Give the extent of all Trypanosoma brucei.
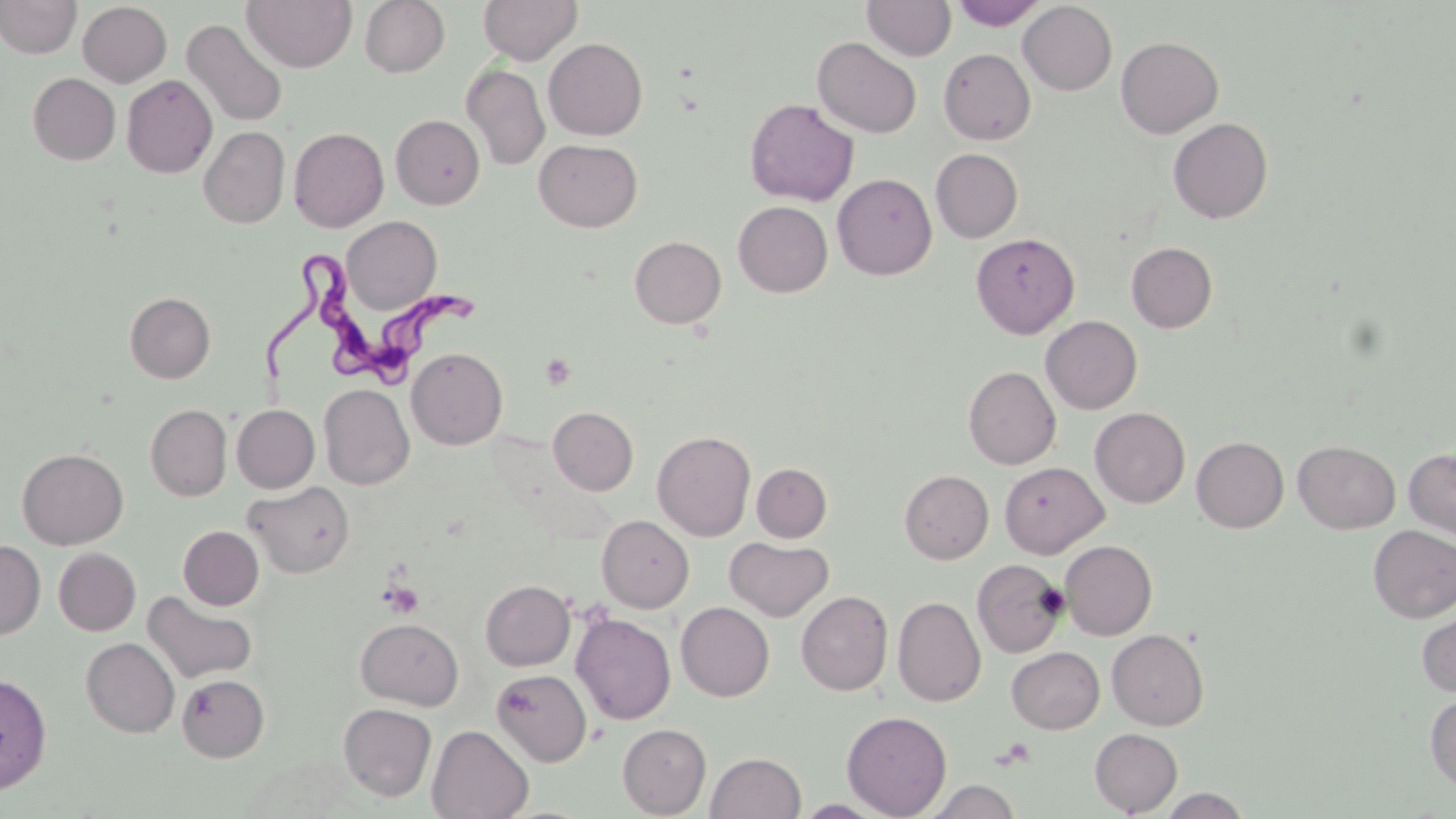

Approximate bounding boxes as (x1,y1)-(x2,y2) corner pairs in pixels.
Trypanosoma brucei: (256,257)-(480,387).

slide-level diagnosis = Trypanosoma brucei
modality = optical microscopy
preparation = thin blood smear
platelet locations = approximate bounding boxes as (x1,y1)-(x2,y2) corner pairs in pixels: (541,354)-(577,389), (380,581)-(424,619)
field of view = single
stain = May-Grünwald-Giemsa
magnification = 1000x
image size = 1456×819 pixels
uninfected red blood cell locations = approximate bounding boxes as (x1,y1)-(x2,y2) corner pairs in pixels: (0,0)-(81,59), (242,0)-(357,72), (360,0)-(450,77), (478,0)-(582,65), (862,0)-(956,61), (951,0)-(1048,30), (77,1)-(172,86), (1018,2)-(1117,95), (181,19)-(288,128), (1116,36)-(1224,138), (813,37)-(922,138), (543,38)-(648,140), (938,48)-(1035,144), (461,63)-(550,170), (28,73)-(120,164), (122,75)-(217,178), (745,98)-(859,206), (391,115)-(485,209), (1168,118)-(1273,223), (199,127)-(290,228), (289,127)-(388,232), (533,138)-(642,232), (931,148)-(1023,243), (832,173)-(936,280), (733,201)-(832,297), (341,216)-(442,314), (971,232)-(1079,339), (629,236)-(726,328), (1126,242)-(1218,333), (125,292)-(215,383), (1041,316)-(1142,414), (406,347)-(507,449), (963,366)-(1061,469), (319,383)-(414,490), (146,404)-(231,501), (232,404)-(320,493), (548,407)-(638,495), (1090,407)-(1190,508), (652,430)-(756,540), (1192,437)-(1289,532), (1293,441)-(1400,533), (1404,447)-(1456,540), (17,448)-(128,549), (999,462)-(1108,557), (751,463)-(832,542), (899,470)-(993,564), (243,481)-(355,578), (596,515)-(694,613), (1368,525)-(1456,623), (178,526)-(263,610), (726,537)-(833,622), (0,540)-(45,639), (1060,540)-(1157,639), (53,547)-(140,635), (971,559)-(1067,658), (480,579)-(575,670), (796,590)-(893,695), (143,591)-(257,684), (893,596)-(986,706), (675,601)-(774,701), (1417,608)-(1456,697), (571,613)-(676,725), (355,617)-(463,710), (1107,629)-(1209,730), (81,637)-(179,737), (1007,646)-(1104,733), (492,669)-(592,766), (0,672)-(52,793), (177,674)-(269,762), (1425,693)-(1456,791), (338,703)-(437,801), (842,710)-(952,818), (617,723)-(711,817), (427,725)-(534,818), (1090,728)-(1182,815), (706,752)-(805,819), (925,779)-(1022,819), (1160,788)-(1250,818), (791,799)-(891,818)